Assess this cell for malaria.
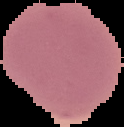
It is uninfected.

image size = 124×127 pixels
image type = cell region segmented out of the field of view; surrounding area masked to black
preparation = thin blood smear